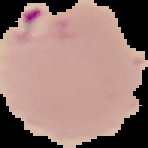

Cell region segmented out of the field of view; the surrounding area is masked to black. From a thin blood film. Image is 148×148 pixels. Result: malaria parasites identified.